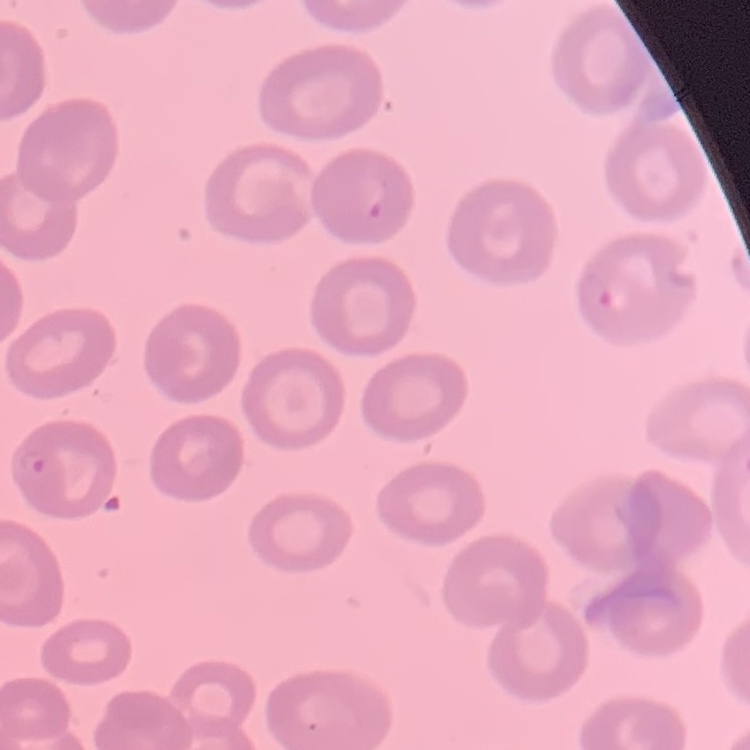
{
  "erythrocyte_morphology": "no rouleaux formation",
  "stain": "Field's or Giemsa",
  "image_type": "square crop of a larger photomicrograph",
  "preparation": "thin peripheral smear"
}